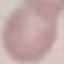 Malaria status: uninfected. Thin blood film. Cell patch, automatically extracted from a larger field of view and resized to 64 × 64 pixels. Photographed with a smartphone camera at the microscope eyepiece. Giemsa-stained preparation.